Identify the parasite.
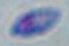

Toxoplasma gondii.

Summary:
  - Magnification: 1000x
  - Modality: photomicrograph